Locate every malaria parasite.
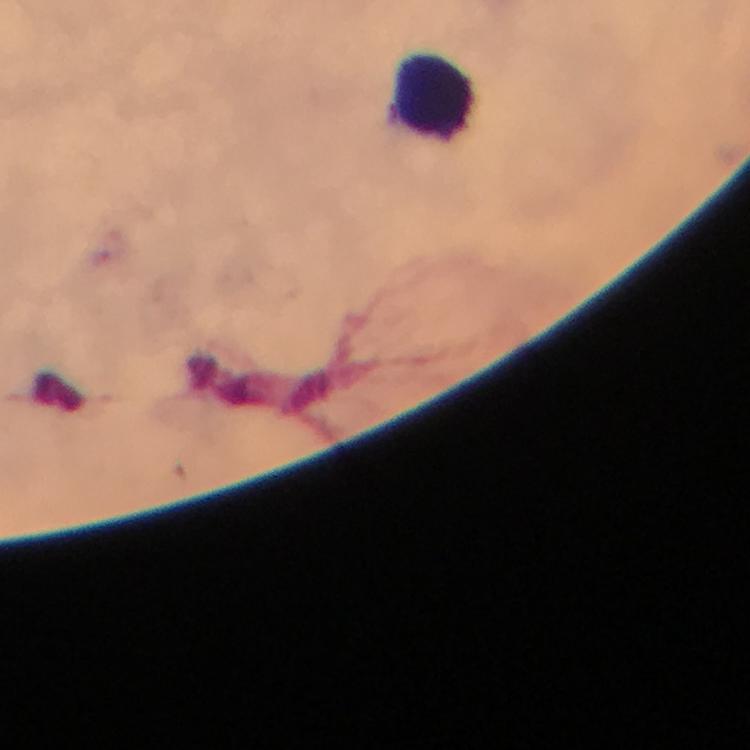

No malaria parasites detected.

image size = 750×750 pixels
cropped from = one field of view
immersion oil = applied
context = from a malaria diagnostic workup
capture = smartphone camera through the microscope
stain = Giemsa
leukocyte locations = approximate centers as [x, y] in pixels: [437, 96]
preparation = thick blood smear
magnification = 100x